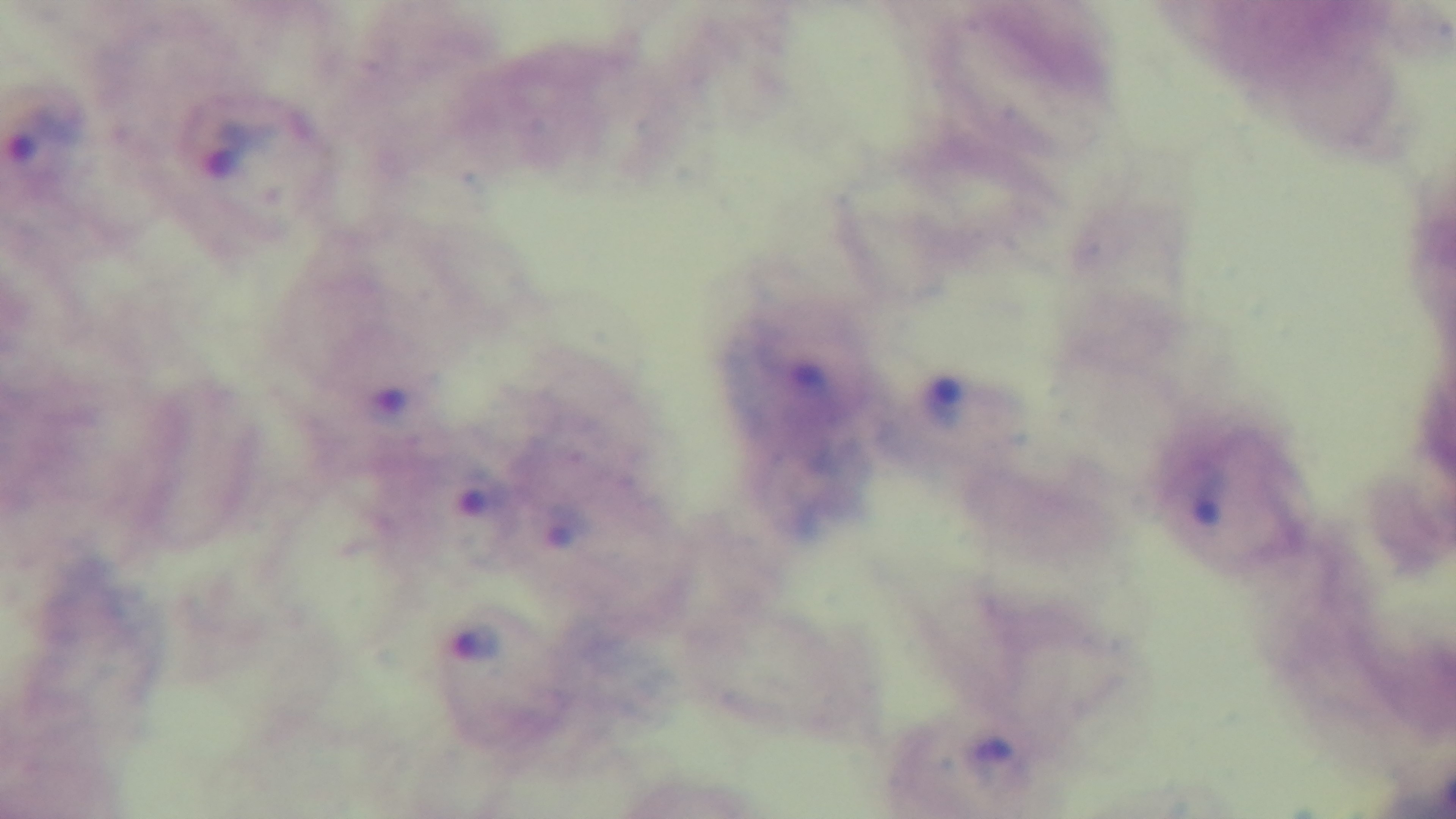
Single field of view. Oil-immersion objective, 100x. Preparation: thick smear. Malaria status: positive. Photomicrograph. Giemsa stain. Captured with a mounted 4K digital camera.